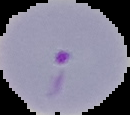

From a thin blood film. Result: Plasmodium parasites identified. Segmented cell region on a black background. Image is 130×115 pixels.